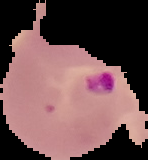
Summary:
  - Image size: 148×160 pixels
  - Preparation: thin blood film
  - Image type: segmented cell region on a black background
  - Result: Plasmodium parasites detected